State the blood parasite species.
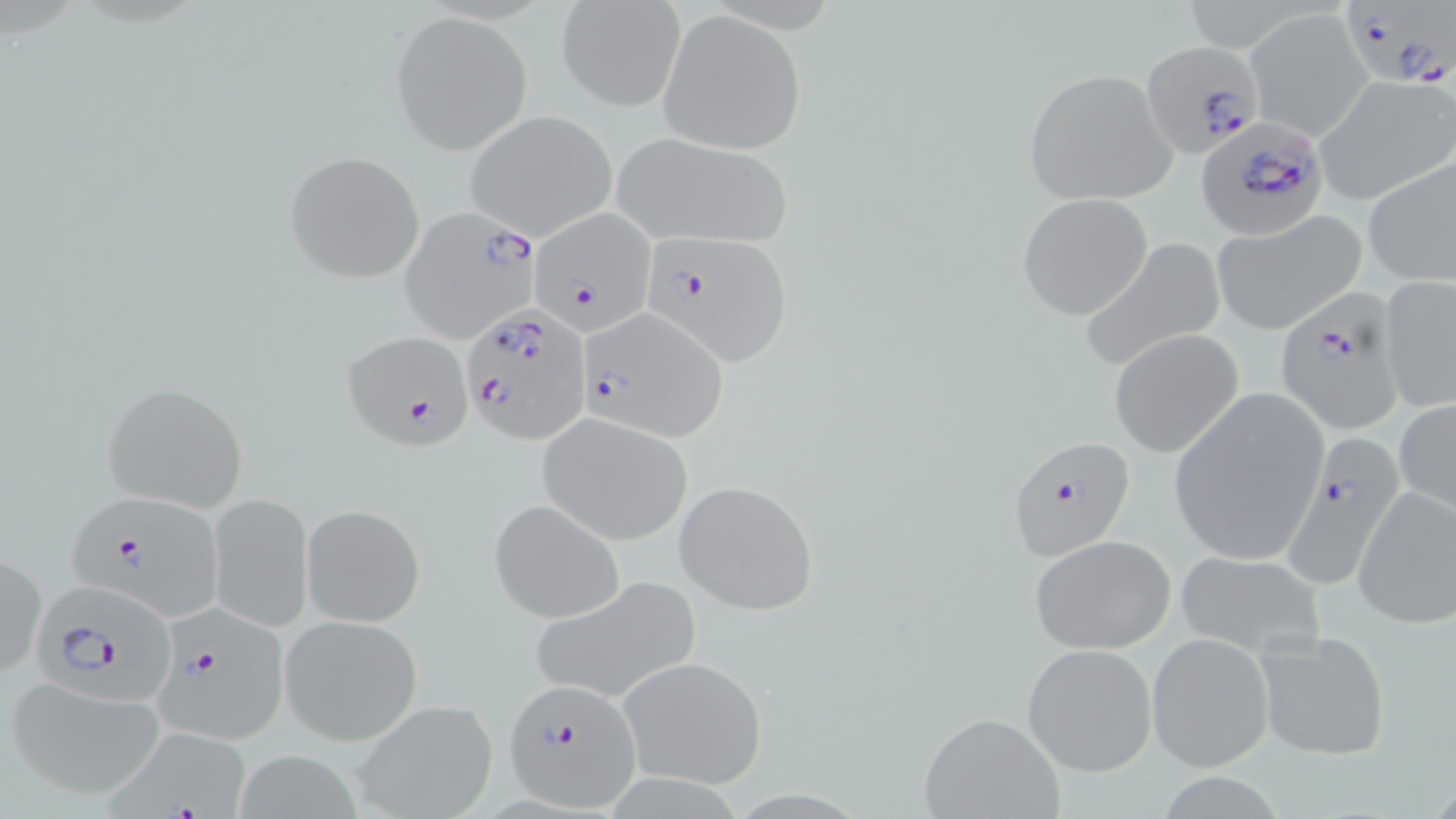

Plasmodium falciparum.

Approximate bounding boxes as (x1,y1)-(x2,y2) corner pairs in pixels. Plasmodium falciparum-infected red blood cell locations: (1335,4)-(1454,90), (1140,40)-(1266,157), (1194,115)-(1326,240), (402,206)-(543,339), (528,209)-(656,331), (639,232)-(795,364), (1274,294)-(1404,433), (460,303)-(592,444), (577,307)-(728,438), (344,331)-(475,449), (1282,433)-(1405,591), (1010,435)-(1138,560), (70,497)-(224,618), (31,583)-(180,708), (157,610)-(292,743), (503,679)-(642,811), (95,723)-(268,819). Uninfected red blood cell locations: (557,1)-(683,112), (659,9)-(807,154), (1247,9)-(1372,139), (393,12)-(531,154), (1024,69)-(1177,204), (1315,75)-(1455,205), (464,111)-(618,241), (609,131)-(795,248), (284,150)-(424,282), (1362,156)-(1455,288), (1017,192)-(1155,321), (1211,213)-(1366,334), (1079,239)-(1228,370), (1379,277)-(1456,413), (1108,329)-(1242,458), (100,380)-(249,511), (1166,388)-(1330,567), (1394,398)-(1456,516), (536,411)-(694,545), (674,480)-(820,614), (1351,487)-(1456,629), (209,493)-(312,630), (488,498)-(625,624), (301,502)-(426,627), (1028,534)-(1175,652), (0,548)-(45,682), (1171,548)-(1324,654), (529,575)-(702,704), (281,615)-(422,744), (1253,628)-(1392,760), (1147,633)-(1275,770), (1023,642)-(1157,775), (616,655)-(768,789), (6,674)-(167,800), (352,699)-(497,819), (919,711)-(1065,819), (232,748)-(379,819). Single field of view. Image is 1456×819 pixels. 1000x magnification. Light microscopy. May-Grünwald-Giemsa stain. Thin blood smear.